Identify the parasite.
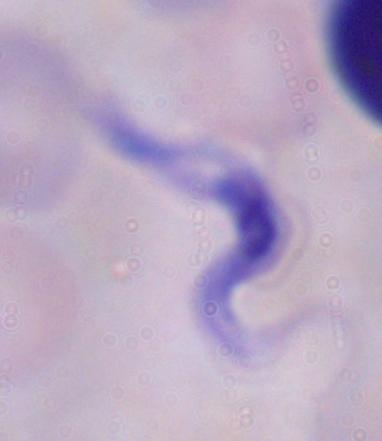
This is a trypanosome.

{
  "modality": "photomicrograph",
  "magnification": "1000x"
}